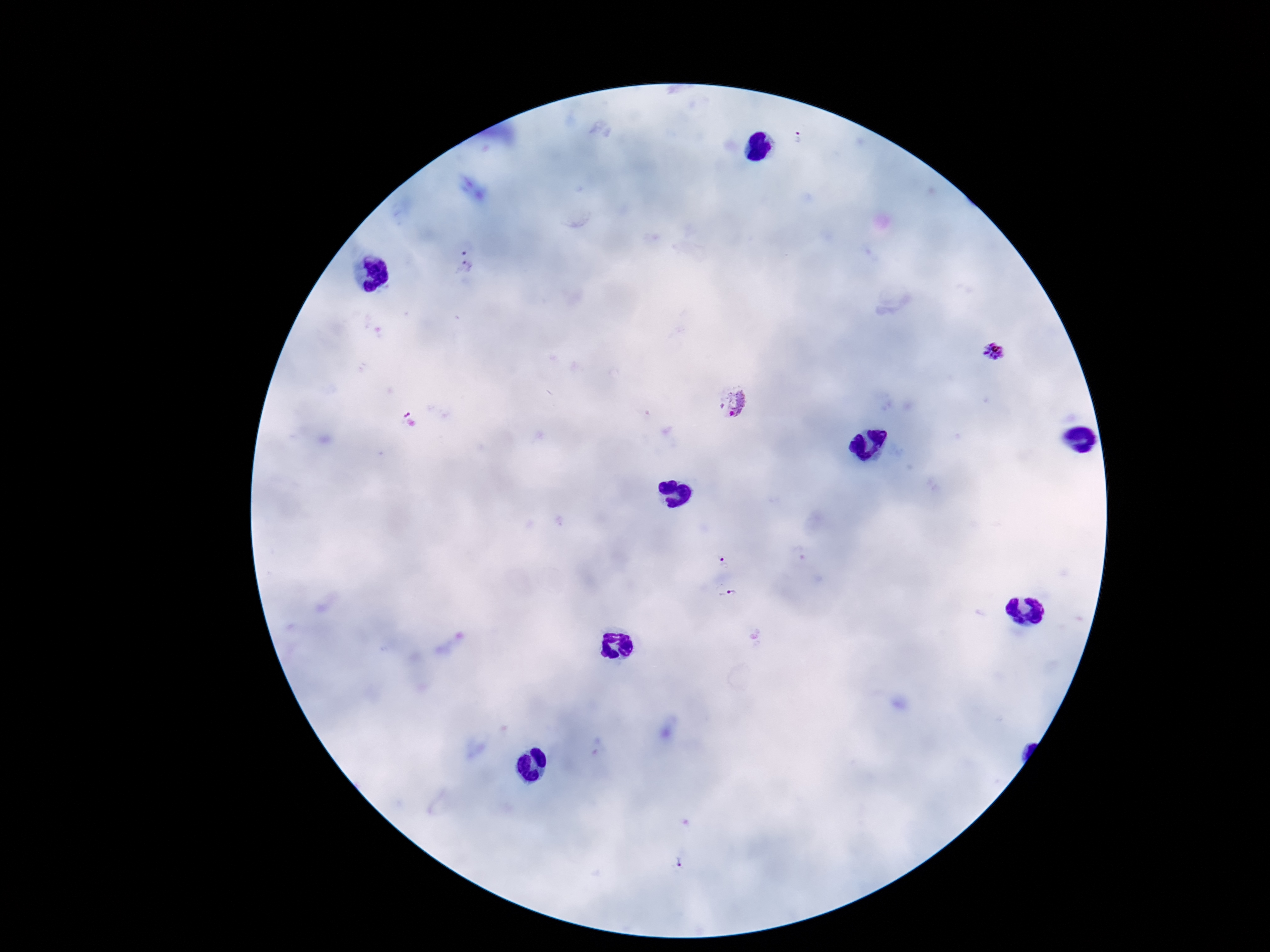
Approximate centers as [x, y] in pixels. Plasmodium parasite locations: [464, 266], [995, 353], [730, 404], [721, 555], [731, 596], [681, 860]. Patient malaria status: infected. Single field of view. Photographed through the microscope eyepiece with a smartphone camera. Image is 1270×952 pixels. 100x magnification. Giemsa stain. Thick peripheral-blood smear.